Name the blood parasite species.
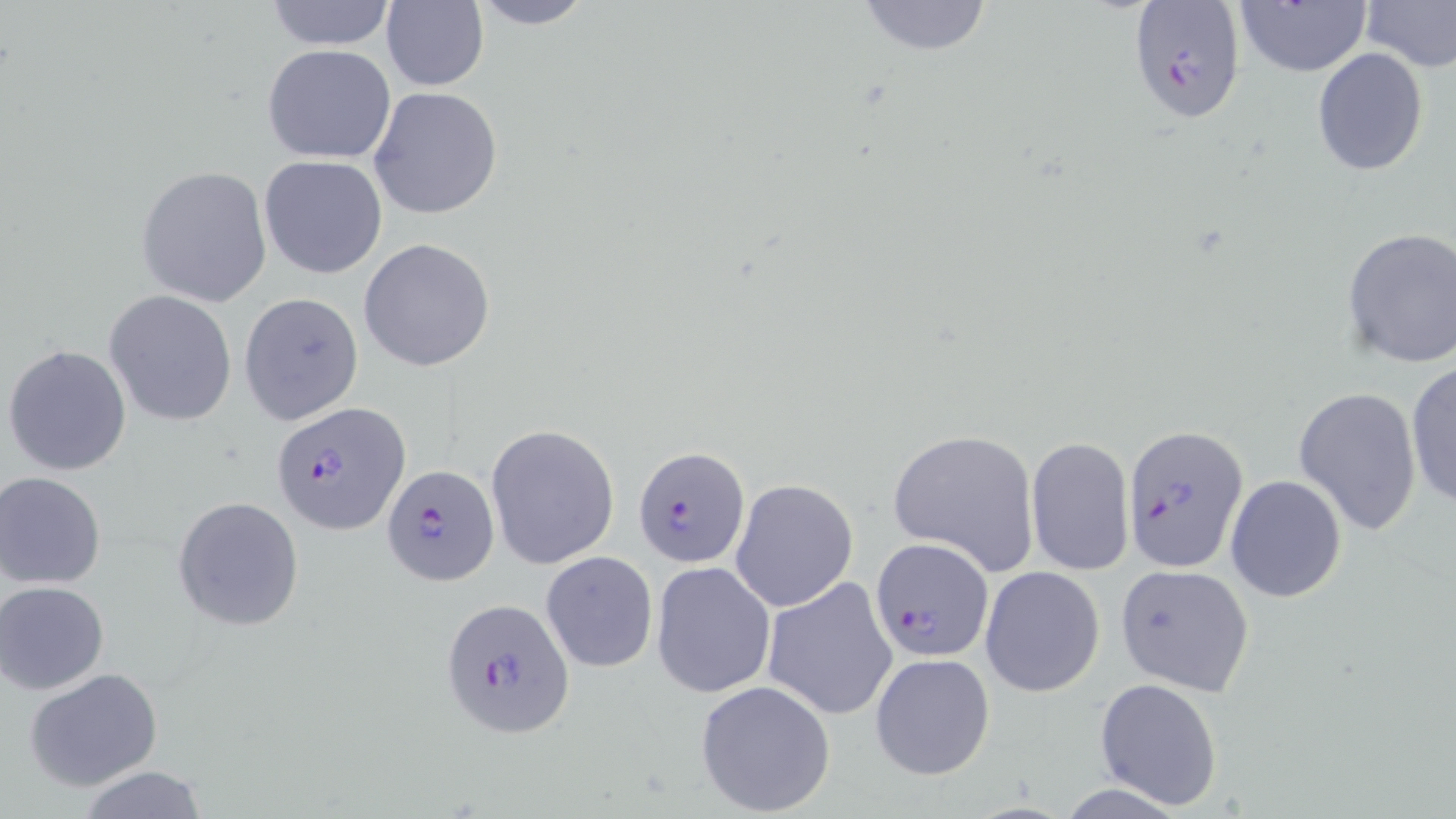
Plasmodium falciparum.

Approximate bounding boxes as [x1, y1, x2, y2] in pixels. Uninfected red blood cell locations: [262, 0, 399, 51], [465, 0, 599, 30], [853, 0, 996, 57], [1358, 0, 1456, 72], [1231, 1, 1371, 78], [380, 2, 489, 91], [263, 43, 396, 164], [1311, 48, 1430, 176], [370, 86, 504, 220], [259, 154, 388, 279], [136, 165, 273, 308], [1340, 227, 1456, 369], [358, 238, 496, 372], [105, 292, 236, 426], [238, 292, 363, 425], [3, 343, 132, 477], [1405, 360, 1455, 510], [1292, 385, 1422, 537], [486, 423, 620, 569], [886, 426, 1040, 575], [1026, 436, 1136, 580], [1, 471, 110, 589], [1224, 474, 1347, 603], [730, 478, 858, 615], [173, 496, 305, 631], [542, 551, 657, 674], [651, 560, 776, 698], [1115, 562, 1255, 695], [981, 567, 1104, 696], [761, 575, 898, 721], [1, 580, 113, 695], [870, 653, 994, 779], [24, 668, 164, 790], [1094, 678, 1225, 811], [694, 679, 838, 816], [71, 767, 211, 819]. Plasmodium falciparum-infected red blood cell locations: [1129, 0, 1246, 127], [272, 401, 410, 535], [1120, 424, 1246, 574], [631, 444, 751, 570], [380, 465, 498, 587], [870, 539, 995, 663], [439, 597, 575, 737]. Thin blood film. 1000x magnification. May-Grünwald-Giemsa stain. Light microscopy. One field of a larger specimen. Image is 1456×819 pixels.